Describe the morphology of the erythrocytes.
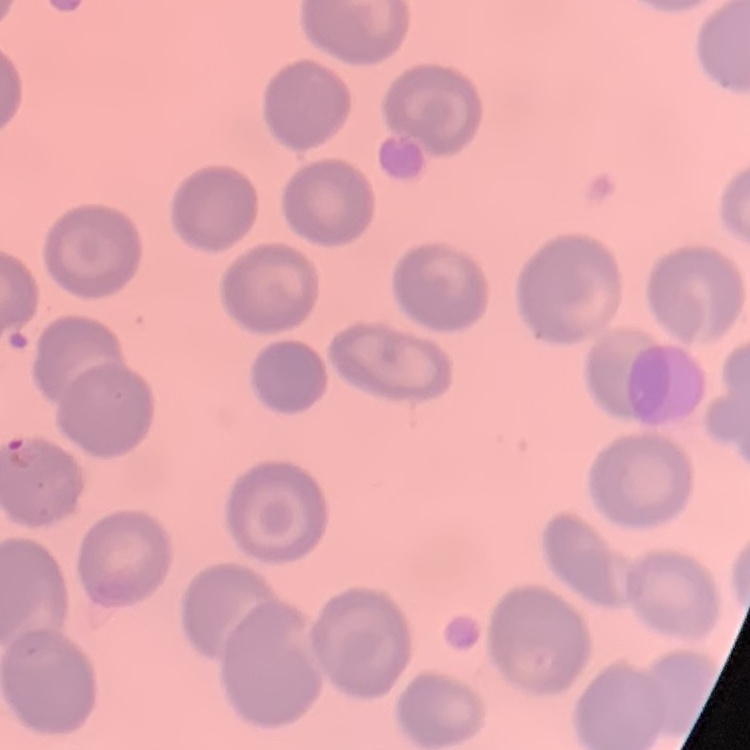
No rouleaux formation.

stain = Field's or Giemsa
preparation = thin blood smear
image type = one tile cut from a larger photomicrograph